Assess this cell for malaria.
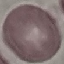

It is uninfected.

preparation = thin smear
stain = Giemsa
capture = smartphone through the microscope eyepiece
image type = cell patch, automatically extracted from a larger field of view and resized to 64 × 64 pixels